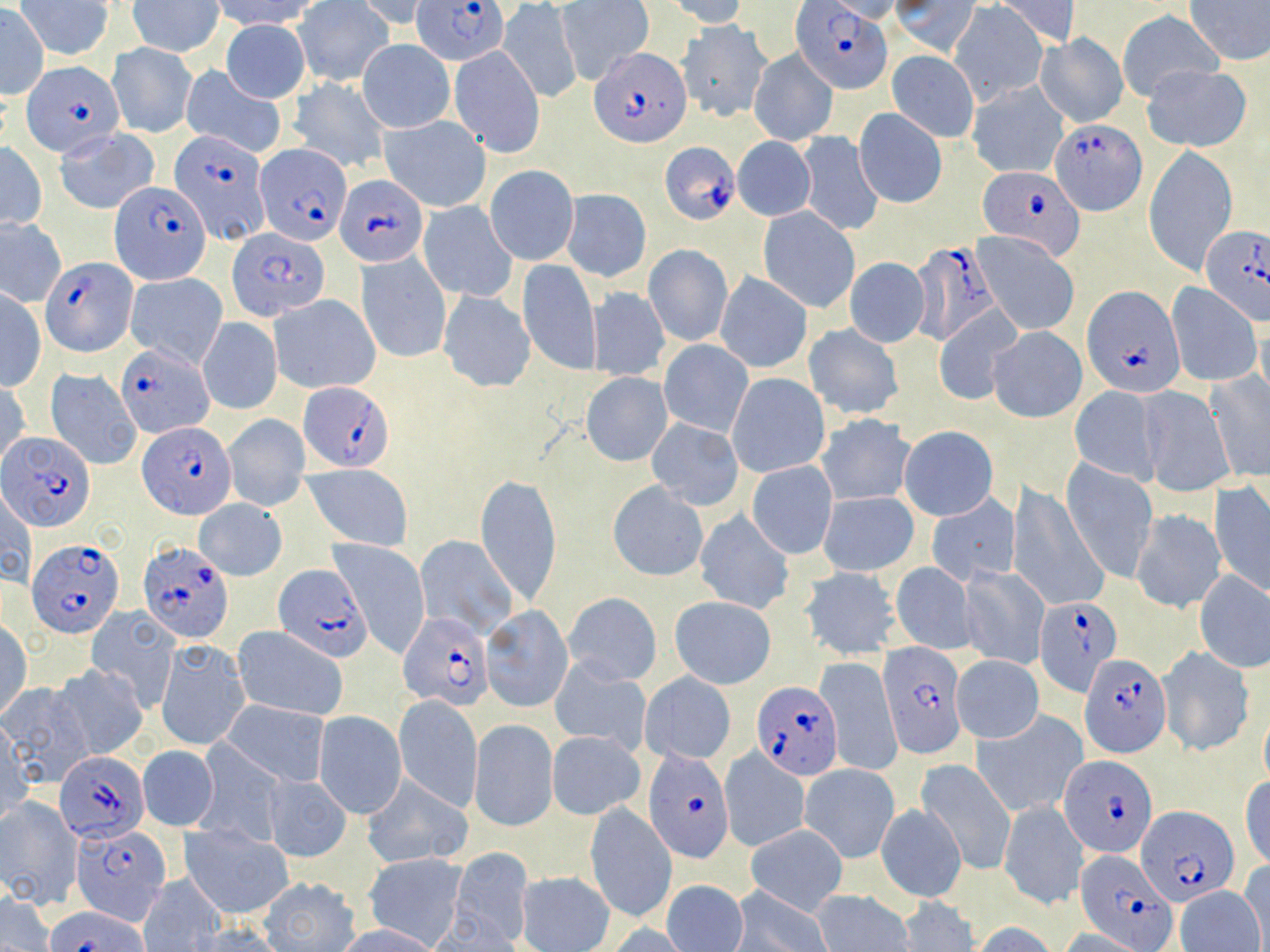
plasmodium_falciparum_infected_red_blood_cell_locations: 'approximate bounding boxes as (x1,y1)-(x2,y2) corner pairs in pixels: (413,0)-(511,66), (792,2)-(891,94), (590,47)-(692,148), (21,62)-(125,156), (1052,118)-(1145,216), (165,128)-(267,242), (660,141)-(742,223), (256,143)-(351,245), (976,166)-(1085,258), (337,174)-(428,267), (111,179)-(210,282), (1199,227)-(1270,327), (229,229)-(327,320), (909,240)-(1001,345), (40,256)-(135,355), (1085,287)-(1185,397), (117,343)-(215,436), (297,382)-(395,472), (139,422)-(235,517), (2,433)-(93,532), (28,537)-(124,636), (138,540)-(234,642), (274,564)-(369,660), (1033,595)-(1125,698), (400,613)-(492,708), (880,646)-(967,759), (1081,651)-(1171,755), (754,682)-(843,778), (646,750)-(734,862), (55,752)-(148,843), (1061,754)-(1156,857), (1139,805)-(1239,905), (73,825)-(170,918), (1079,847)-(1178,950), (46,904)-(149,952)'
slide_level_diagnosis: Plasmodium falciparum
preparation: thin blood smear
image_size: 1270×952 pixels
uninfected_red_blood_cell_locations: 'approximate bounding boxes as (x1,y1)-(x2,y2) corner pairs in pixels: (213,0)-(320,32), (663,0)-(750,28), (994,0)-(1080,49), (1184,0)-(1270,67), (128,1)-(223,56), (352,1)-(437,32), (557,1)-(654,85), (820,1)-(907,22), (891,1)-(980,56), (949,1)-(1049,106), (16,2)-(114,61), (293,2)-(392,86), (499,2)-(582,103), (0,7)-(48,97), (1117,10)-(1223,104), (221,20)-(310,102), (679,21)-(772,122), (1037,34)-(1127,129), (358,38)-(454,134), (107,42)-(197,138), (450,45)-(545,157), (748,48)-(839,148), (886,50)-(979,143), (1141,64)-(1252,151), (181,65)-(287,158), (287,76)-(392,174), (966,80)-(1069,179), (854,107)-(947,207), (379,115)-(492,212), (55,129)-(159,214), (796,132)-(884,237), (732,137)-(816,222), (1,142)-(47,230), (1144,146)-(1238,274), (484,165)-(579,265), (562,189)-(651,283), (418,201)-(518,302), (758,207)-(861,313), (1,218)-(67,306), (973,233)-(1079,335), (644,245)-(733,347), (356,252)-(452,363), (518,258)-(601,375), (845,259)-(930,348), (127,272)-(227,368), (715,272)-(812,373), (1166,284)-(1261,387), (587,287)-(670,381), (0,289)-(45,391), (438,291)-(535,392), (269,295)-(380,394), (933,304)-(1023,405), (198,317)-(282,415), (804,323)-(903,420), (986,326)-(1087,423), (659,341)-(753,436), (45,370)-(143,471), (1206,370)-(1269,481), (581,372)-(672,466), (728,373)-(830,478), (0,382)-(31,469), (1137,387)-(1234,495), (1068,388)-(1162,483), (817,414)-(915,506), (223,415)-(310,512), (647,419)-(744,510), (897,426)-(998,521), (1061,460)-(1158,581), (747,462)-(837,558), (302,464)-(413,550), (476,474)-(560,606), (608,481)-(708,581), (1210,482)-(1270,599), (1010,483)-(1105,613), (2,486)-(35,589), (819,492)-(919,576), (927,494)-(1020,585), (194,499)-(286,580), (1129,509)-(1225,614), (695,511)-(793,615), (416,534)-(519,639), (330,540)-(431,658), (890,561)-(977,653), (958,564)-(1049,670), (799,567)-(900,660), (1195,570)-(1270,673), (562,594)-(662,686), (669,596)-(776,689), (480,606)-(572,712), (85,607)-(181,714), (0,622)-(32,720), (231,627)-(350,722), (157,640)-(250,750), (1157,646)-(1255,756), (952,654)-(1043,742), (817,657)-(901,776), (550,658)-(651,753), (52,663)-(147,760), (640,672)-(736,764), (1,684)-(94,788), (393,695)-(483,811), (222,700)-(331,788), (973,710)-(1087,816), (315,712)-(407,818), (469,720)-(558,832), (1,723)-(34,829), (546,731)-(645,820), (193,739)-(286,846), (139,746)-(218,831), (719,748)-(810,852), (915,759)-(1016,876), (799,763)-(899,862), (262,774)-(352,863), (361,775)-(473,868), (1240,777)-(1270,868), (0,797)-(82,910), (998,798)-(1088,911), (583,804)-(677,924), (876,805)-(965,902), (182,825)-(292,919), (745,825)-(848,916), (449,848)-(535,948), (362,854)-(469,949), (1237,861)-(1270,948), (516,871)-(614,952), (137,874)-(225,951), (256,876)-(362,950), (661,880)-(748,952), (1176,885)-(1264,952), (730,887)-(831,952), (811,890)-(915,951), (2,892)-(56,951), (897,895)-(977,952), (333,923)-(447,952), (604,923)-(690,951), (972,923)-(1059,951), (1059,929)-(1147,952)'
magnification: 1000x
field_of_view: single
modality: light microscopy
stain: May-Grünwald-Giemsa